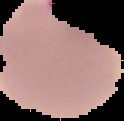
image_size: 124×121 pixels
preparation: thin blood film
image_type: cell region segmented out of the field of view; surrounding area masked to black
malaria_status: parasitized